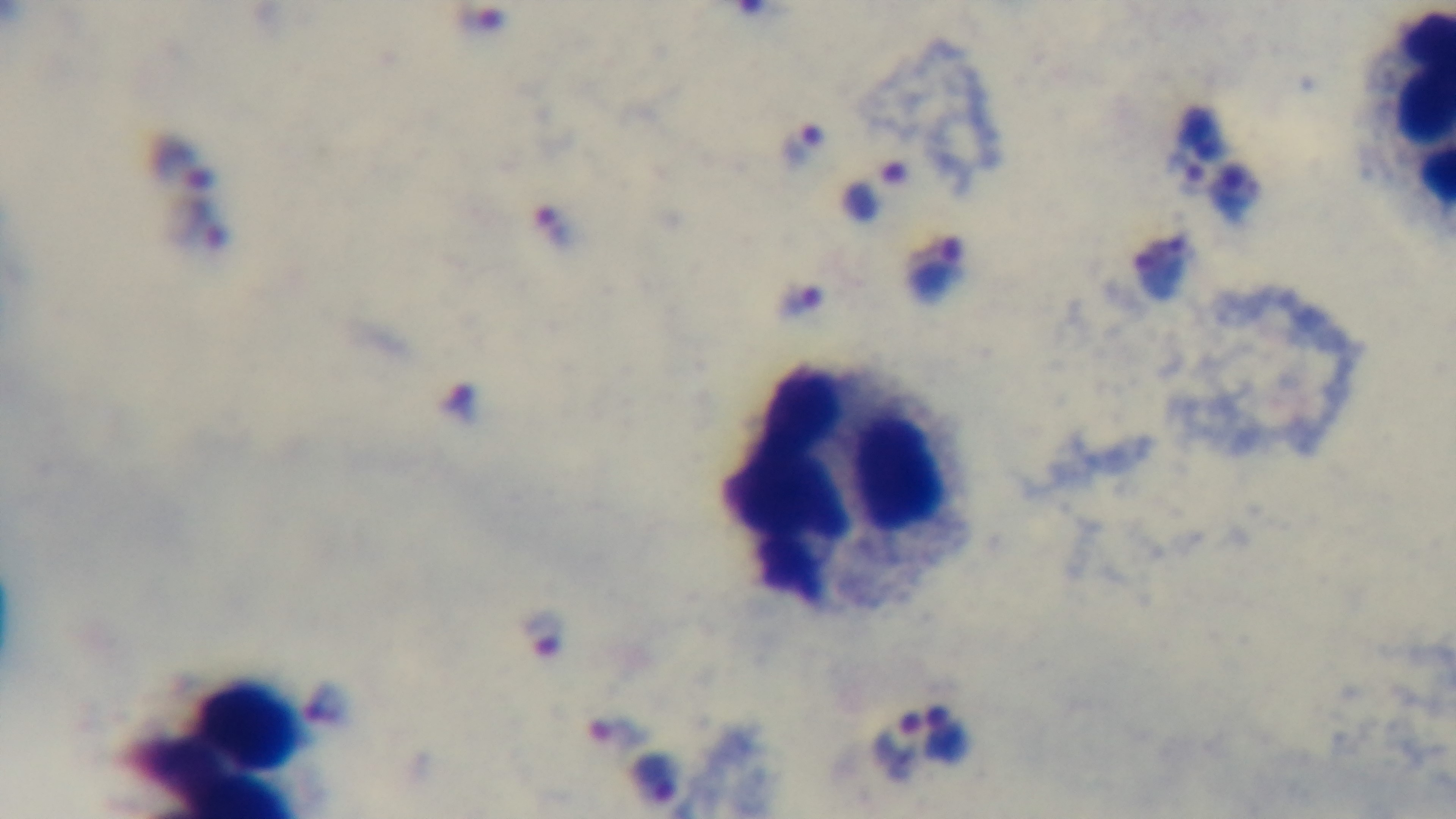

Oil-immersion objective, 100x. One field from the slide. Malaria status: positive. Light microscopy. Preparation: thick smear. Giemsa stain. Mounted 4K digital camera.